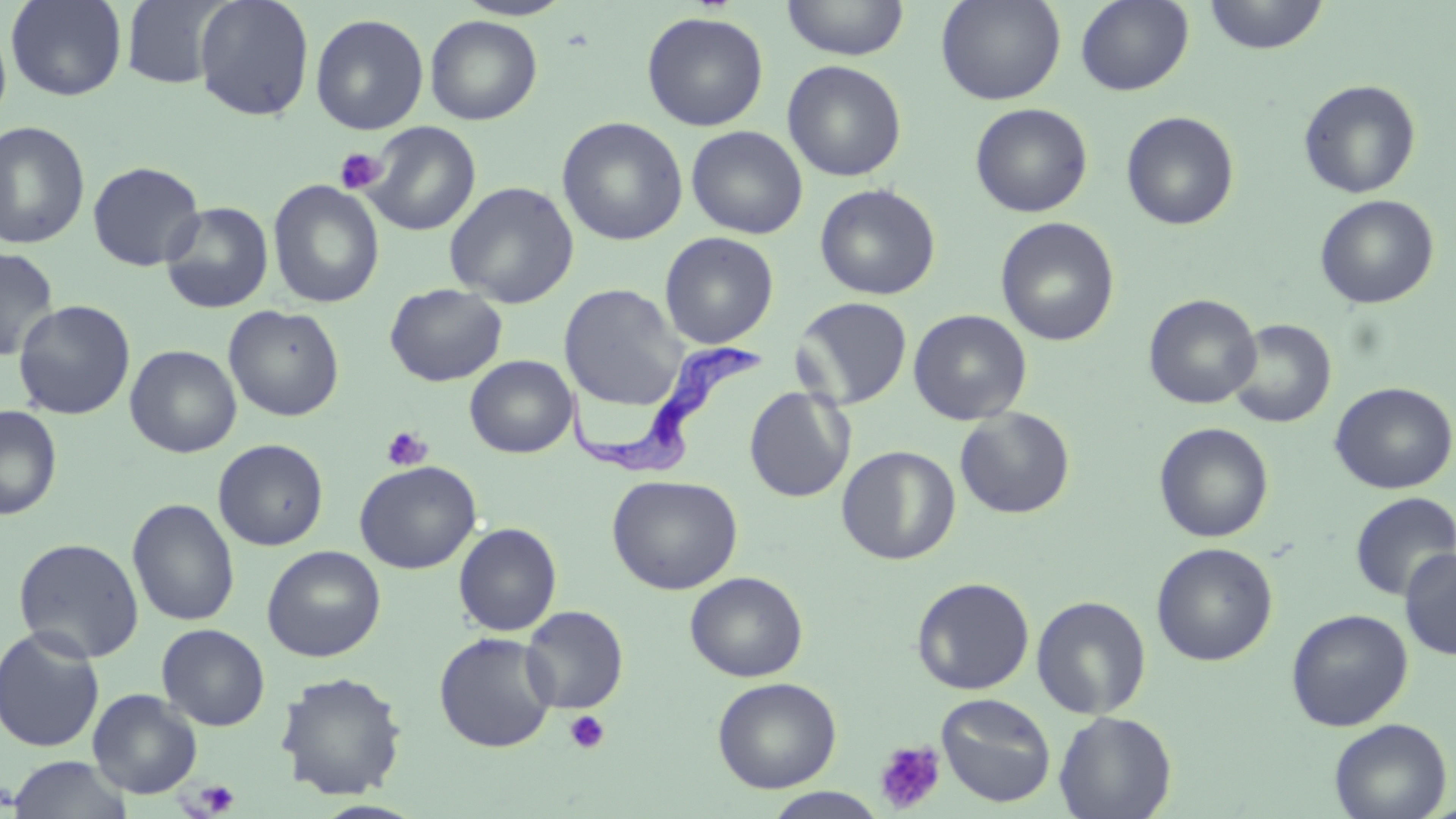
Approximate bounding boxes as (x1,y1)-(x2,y2) corner pairs in pixels. Platelet locations: (334,148)-(386,194), (381,426)-(432,471), (564,710)-(610,754), (875,740)-(945,813), (195,780)-(240,816). Uninfected red blood cell locations: (5,0)-(127,101), (120,0)-(232,89), (194,0)-(315,121), (454,0)-(575,21), (781,0)-(910,61), (936,0)-(1065,105), (1075,0)-(1194,95), (1202,0)-(1329,55), (641,11)-(769,131), (310,13)-(429,135), (0,15)-(12,127), (425,15)-(543,125), (782,60)-(907,181), (1298,79)-(1421,199), (970,103)-(1093,217), (1121,111)-(1239,230), (557,116)-(688,246), (0,120)-(91,250), (362,121)-(480,235), (686,125)-(808,239), (87,161)-(206,271), (267,179)-(384,309), (444,181)-(579,308), (814,183)-(941,300), (1315,195)-(1440,309), (160,201)-(274,314), (995,217)-(1120,346), (660,231)-(779,349), (0,246)-(59,362), (385,283)-(507,387), (559,284)-(686,410), (1143,294)-(1262,409), (792,296)-(913,410), (13,299)-(135,420), (223,304)-(345,422), (908,309)-(1032,425), (1226,319)-(1336,428), (125,344)-(242,458), (464,355)-(577,458), (1329,382)-(1456,494), (744,386)-(855,502), (0,406)-(62,520), (954,407)-(1075,519), (1154,422)-(1274,543), (213,439)-(328,551), (836,445)-(961,565), (354,460)-(482,574), (606,474)-(743,595), (1349,491)-(1456,601), (127,498)-(240,627), (453,522)-(561,636), (13,537)-(145,663), (1151,542)-(1278,666), (261,545)-(386,662), (1399,548)-(1456,660), (684,571)-(808,682), (911,576)-(1034,695), (1031,595)-(1152,719), (521,605)-(628,713), (1285,608)-(1413,731), (156,623)-(270,731), (0,626)-(105,753), (434,632)-(558,753), (274,670)-(408,801), (712,677)-(841,793), (88,689)-(203,798), (936,693)-(1056,808), (1055,710)-(1177,819), (1329,718)-(1452,819), (7,756)-(134,818), (764,788)-(889,818). Trypanosoma brucei locations: (565,342)-(766,478). Slide-level diagnosis: Trypanosoma brucei. May-Grünwald-Giemsa-stained preparation. Light microscopy. One field of a larger specimen. Image is 1456×819 pixels. 1000x magnification. Thin blood smear.